Report the malaria status of this cell.
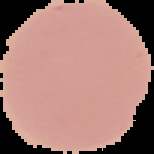
It is uninfected.

Summary:
  - Image size: 154×154 pixels
  - Preparation: thin blood smear
  - Image type: segmented cell region on a black background